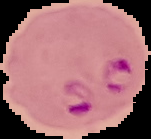
image type = cell region segmented out of the field of view; surrounding area masked to black
image size = 151×139 pixels
preparation = thin blood film
malaria status = parasitized